Assess this cell for malaria.
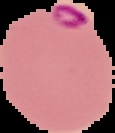

It is parasitized.

Summary:
  - Image type: segmented cell region on a black background
  - Image size: 115×133 pixels
  - Preparation: thin blood film